State which parasite is depicted.
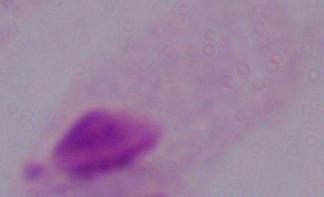

This is a trichomonad.

1000x magnification. Micrograph.